Comment on the morphology of the red blood cells.
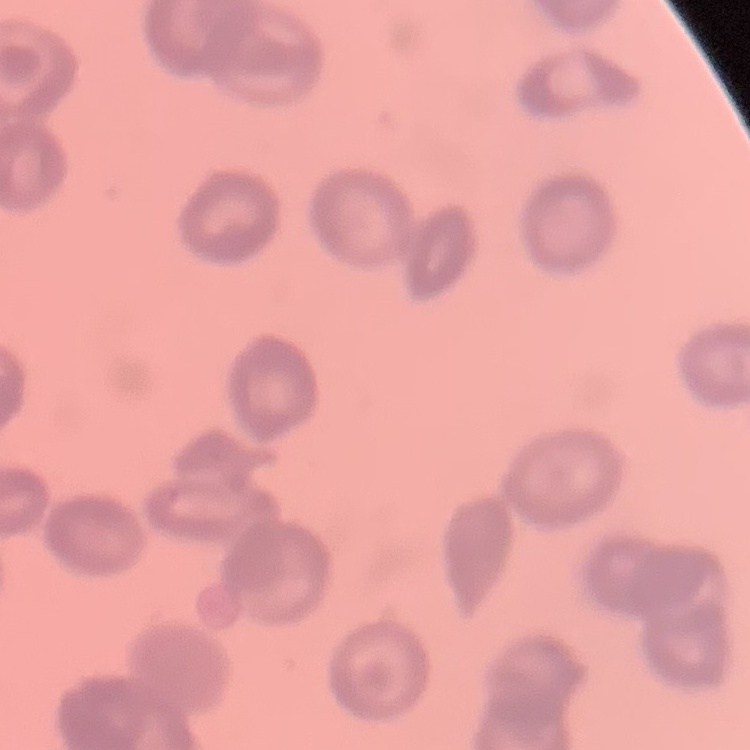

They show rouleaux formation.

Field's or Giemsa stain. One tile cut from a larger photomicrograph. Thin blood film.